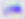 400x magnification. Toxoplasma gondii is seen. Photomicrograph.